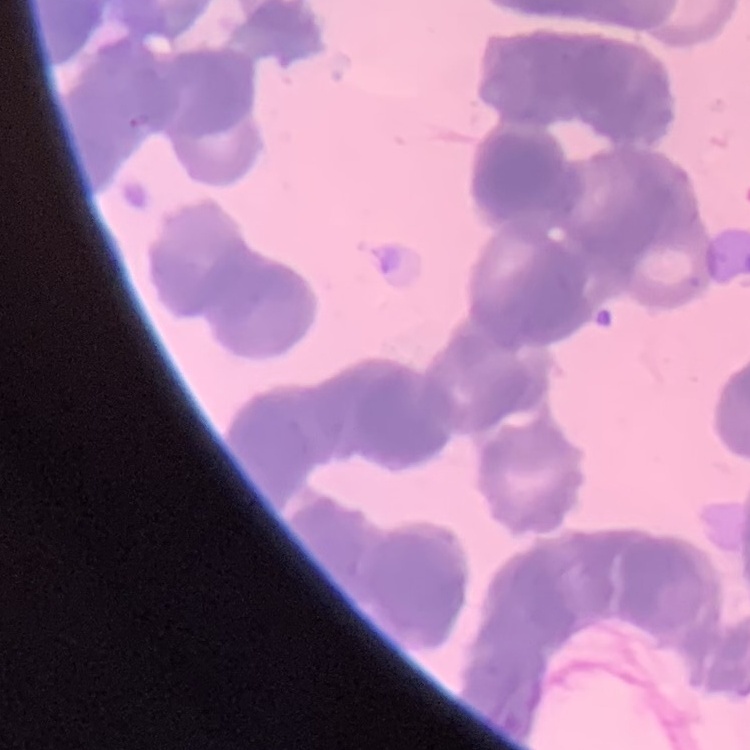

{
  "red_blood_cell_morphology": "rouleaux formation",
  "stain": "Field's or Giemsa",
  "preparation": "thin peripheral smear",
  "image_type": "square crop of a larger photomicrograph"
}